Name the blood parasite species.
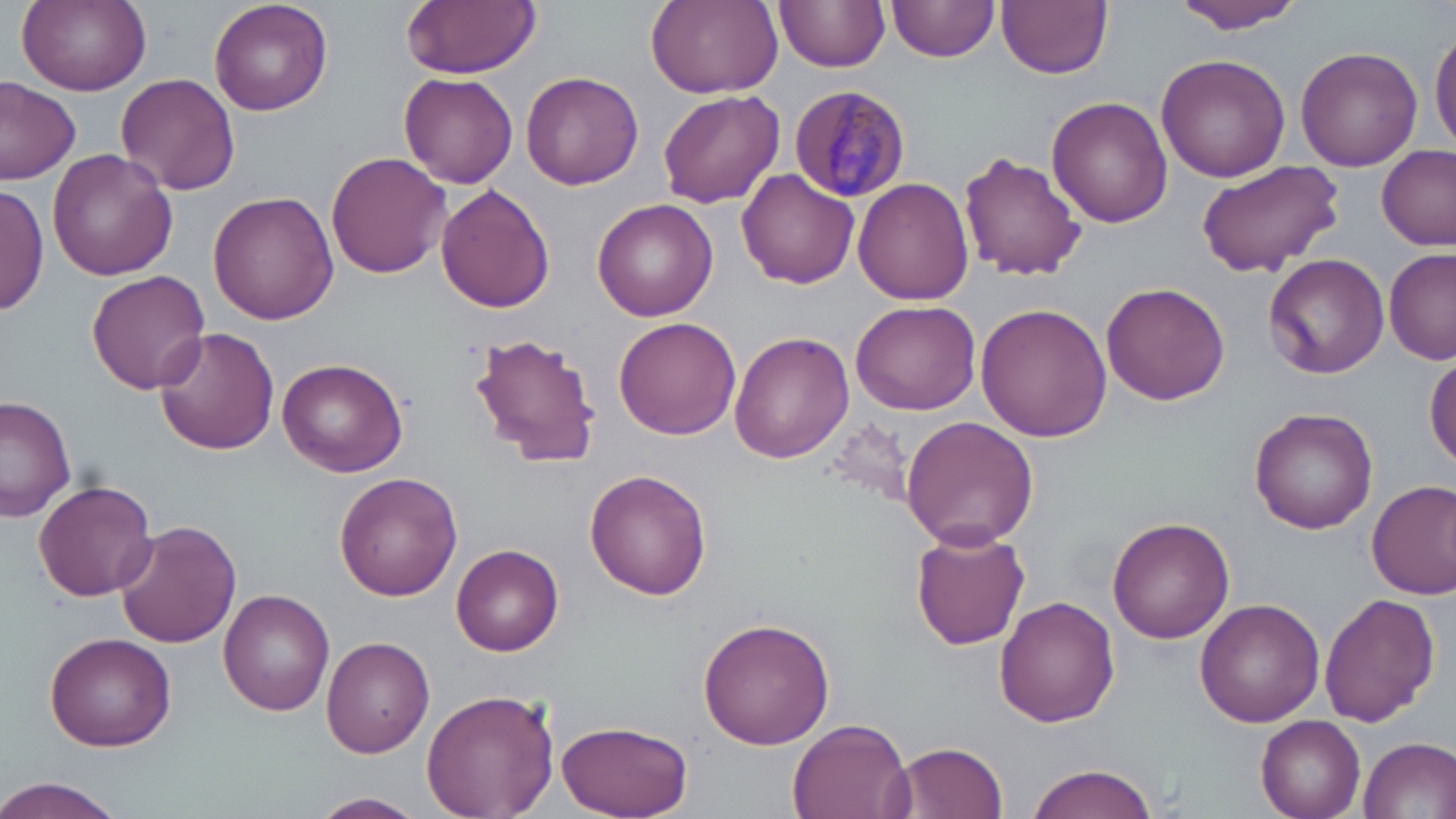
Plasmodium malariae.

Approximate bounding boxes as (x1, y1, x2, y2) in pixels. Uninfected red blood cell locations: (18, 0, 150, 96), (209, 0, 332, 115), (400, 0, 541, 77), (646, 0, 783, 98), (775, 0, 890, 72), (889, 0, 997, 63), (998, 0, 1112, 80), (1171, 0, 1309, 32), (1430, 28, 1456, 152), (1294, 45, 1422, 171), (1156, 54, 1291, 180), (520, 70, 644, 190), (398, 71, 520, 188), (117, 72, 240, 195), (0, 80, 81, 185), (658, 89, 784, 208), (1045, 97, 1173, 228), (77, 116, 225, 268), (1376, 144, 1454, 250), (47, 148, 179, 280), (959, 152, 1088, 281), (326, 153, 449, 278), (1194, 158, 1343, 275), (737, 168, 859, 288), (853, 177, 975, 305), (436, 184, 556, 314), (0, 185, 49, 315), (206, 189, 336, 326), (591, 197, 718, 320), (1384, 248, 1456, 366), (1263, 253, 1389, 380), (87, 270, 210, 394), (1101, 280, 1230, 404), (851, 300, 983, 416), (974, 302, 1113, 441), (615, 318, 741, 440), (154, 326, 280, 456), (730, 331, 853, 465), (471, 333, 603, 467), (1426, 350, 1455, 471), (278, 360, 407, 475), (0, 394, 78, 522), (1250, 408, 1378, 534), (901, 416, 1038, 548), (585, 467, 713, 598), (335, 472, 463, 599), (1366, 478, 1456, 600), (33, 479, 157, 601), (1107, 517, 1234, 644), (114, 519, 242, 648), (911, 530, 1031, 650), (451, 543, 564, 656), (221, 589, 335, 716), (1317, 591, 1440, 726), (994, 596, 1120, 728), (1195, 598, 1326, 726), (698, 616, 836, 750), (44, 632, 177, 751), (320, 636, 435, 757), (421, 688, 558, 819), (1256, 715, 1366, 819), (787, 716, 915, 819), (554, 719, 693, 819), (1359, 736, 1455, 817), (889, 741, 1009, 819), (1023, 763, 1163, 819), (0, 776, 127, 819), (312, 792, 426, 818). Plasmodium malariae-infected red blood cell locations: (785, 82, 910, 201). Single field of view. Captured at 1000x magnification. Optical microscopy. Image is 1456×819 pixels. May-Grünwald-Giemsa stain. Thin blood smear.